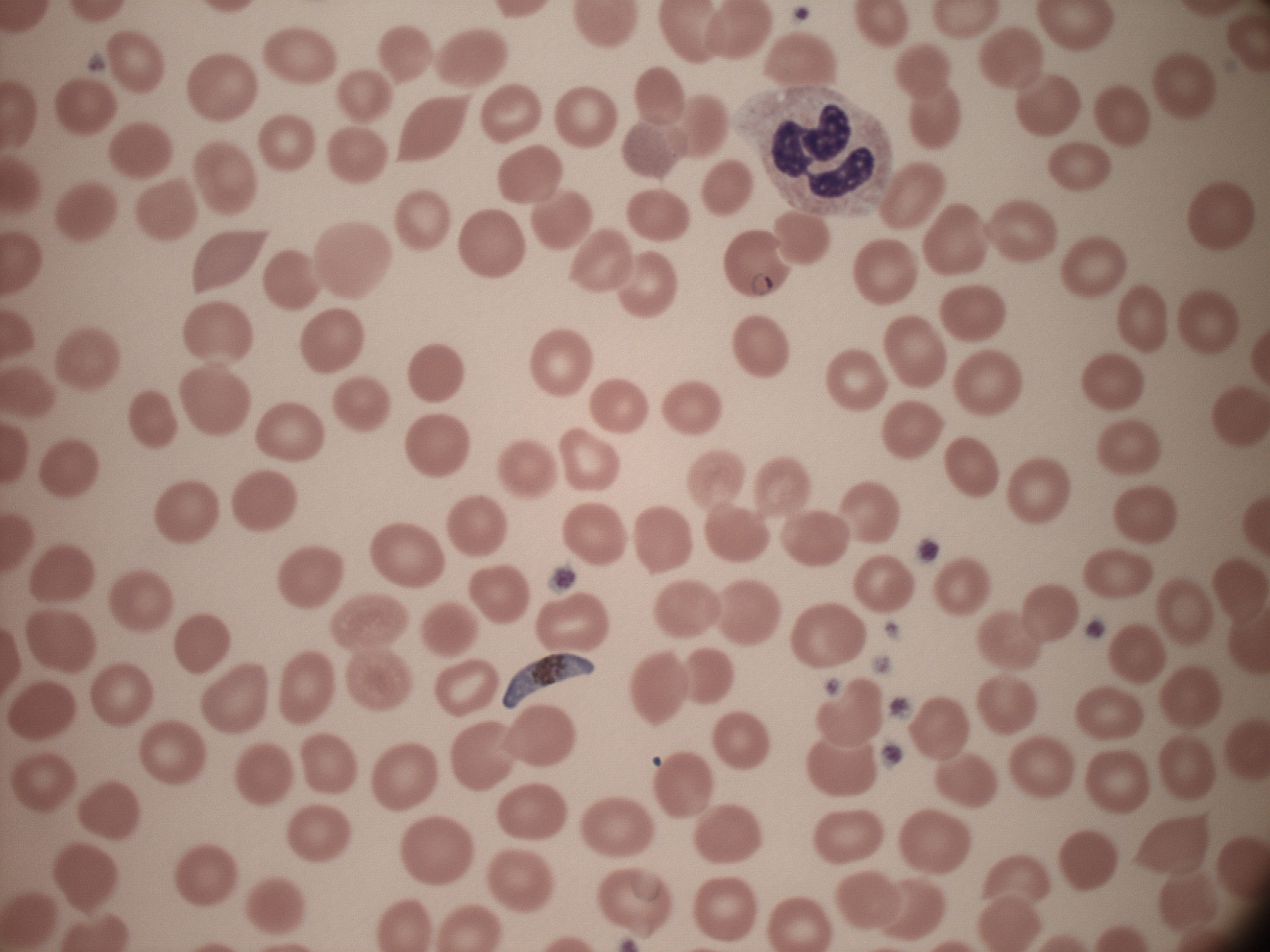 Approximate bounding boxes as (x1, y1, x2, y2) in pixels, from the source annotation, which is not necessarily exhaustive. Ring form locations: (752, 273, 774, 296). Gametocyte locations: (502, 652, 595, 709). Life-cycle stages among the annotated parasites: ring form, gametocyte. Captured at 100x magnification. Giemsa-stained preparation. Thin blood film. Single field of view. Leica DM2000 optical microscope with a built-in camera. Species: Plasmodium falciparum. Image is 1270×952 pixels.